Give the position of each Plasmodium falciparum parasite with its life-cycle stage, each leukocyte, and any debris.
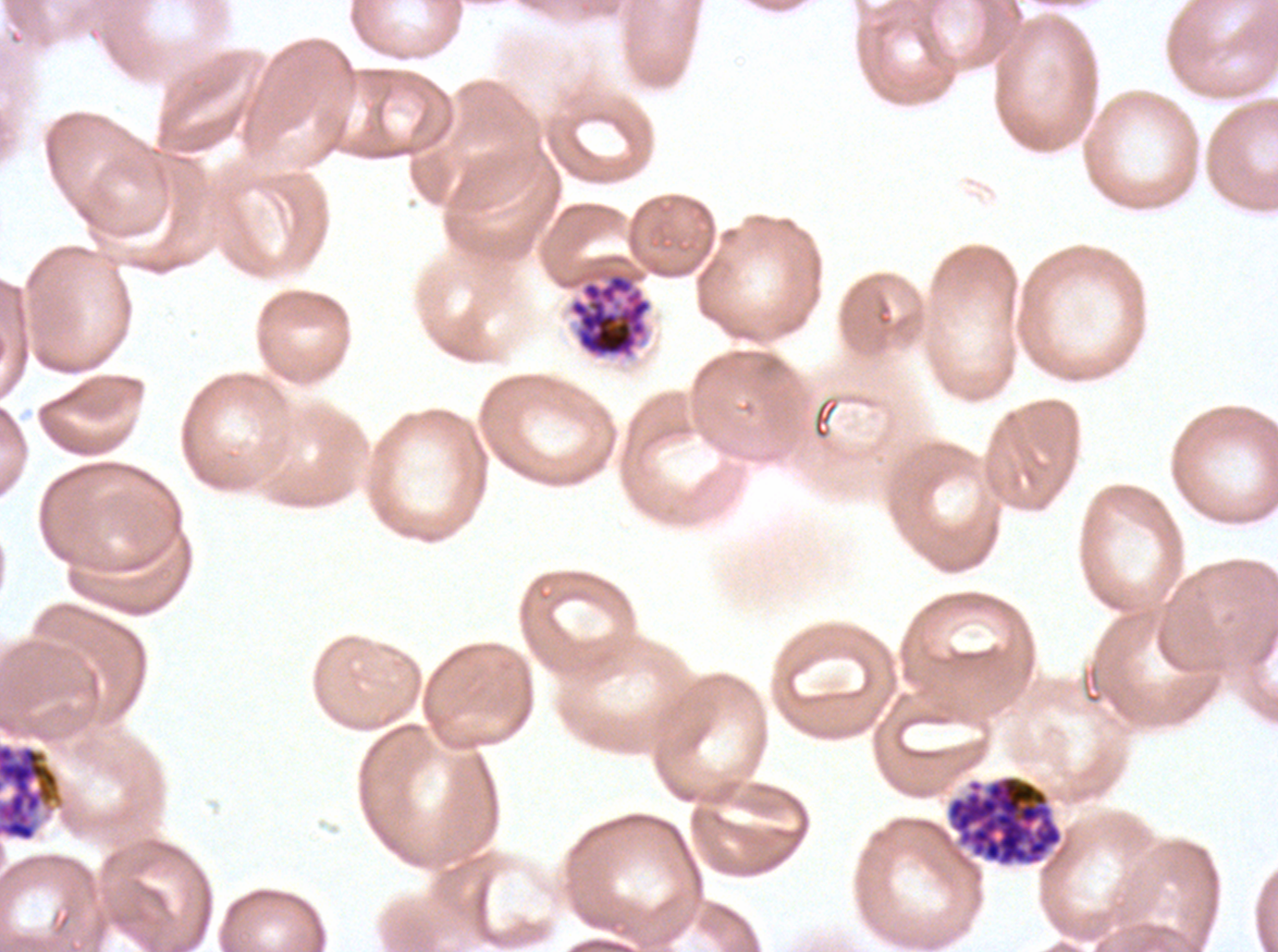
Approximate bounding boxes as {x1, y1, x2, y2} in pixels.
Segmenters: {569, 273, 652, 359}, {0, 741, 68, 843}, {945, 775, 1063, 867}.
No rings, late-ring/early-trophozoite forms, mid trophozoites, late trophozoites, early schizonts, late schizonts, gametocytes, leukocytes, or debris observed.

image size = 1278×952 pixels
specimen = Plasmodium falciparum cultured ex vivo for 24 to 48 hours, from a patient in The Gambia
preparation = thin blood smear
stain = Giemsa
field of view = one sub-image of a larger composite